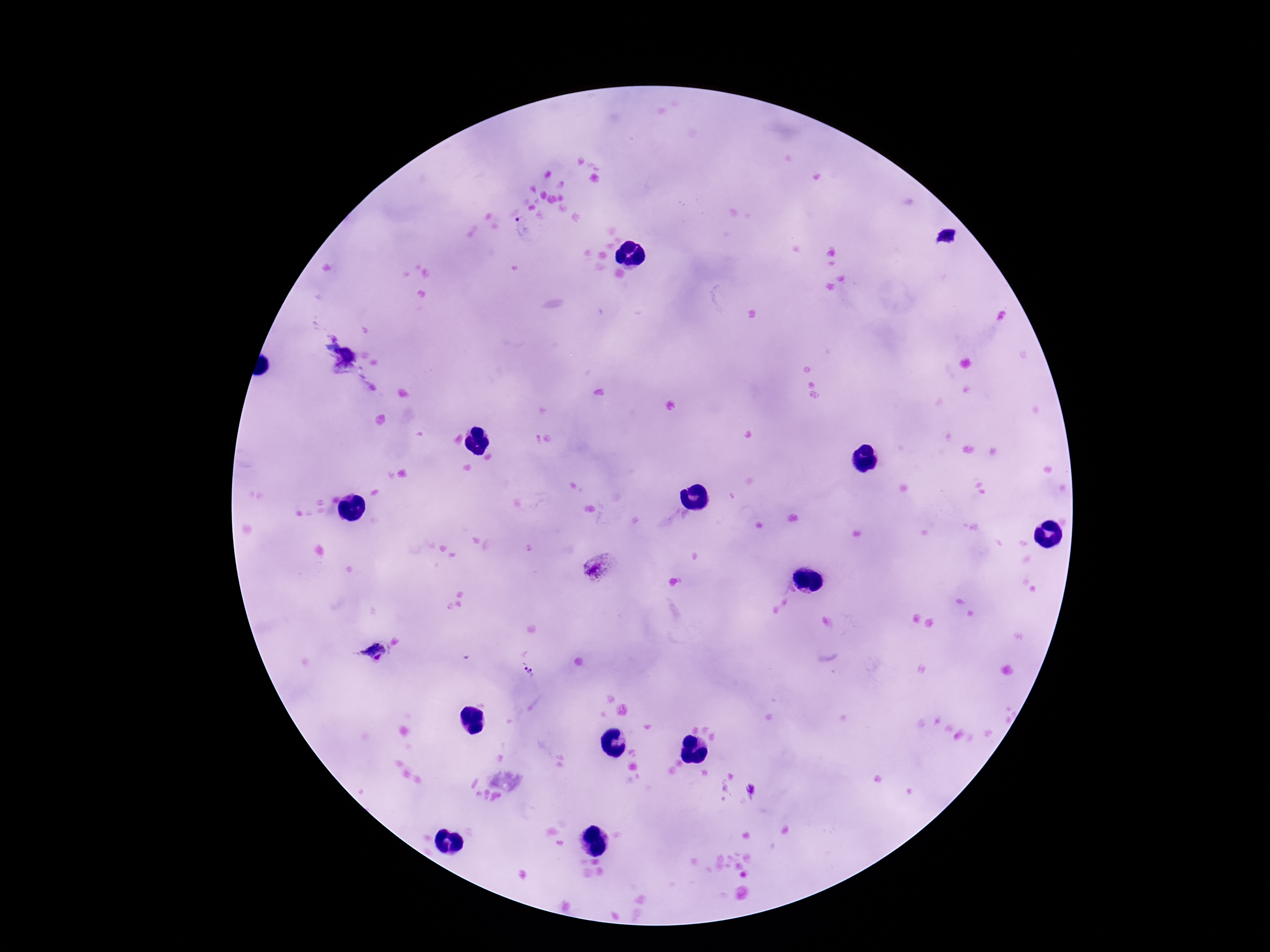

Approximate centers as {x, y} in pixels. Plasmodium parasite locations: {523, 229}, {599, 567}, {371, 650}, {528, 669}, {751, 790}. Single field of view. Thick blood film. Smartphone photograph taken through the microscope eyepiece. Giemsa stain. 100x magnification. Patient malaria status: positive. Image is 1270×952 pixels.